Classify this cell by malaria status.
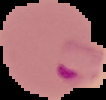

It is parasitized.

Summary:
  - Image size: 106×100 pixels
  - Image type: cell region segmented out of the field of view; surrounding area masked to black
  - Preparation: thin blood film